Assess this cell for malaria.
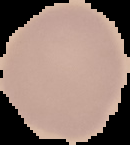

It is uninfected.

From a thin blood smear. Image is 130×145 pixels. The area outside the segmented cell region is set to black.